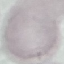

malaria status = uninfected
capture = smartphone through the microscope eyepiece
stain = Giemsa
preparation = thin blood film
image type = cell patch, automatically extracted from a larger field of view and resized to 64 × 64 pixels